Classify this cell by malaria status.
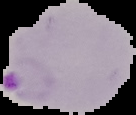

It is parasitized.

Summary:
  - Image type: segmented cell region with the area outside set to black
  - Image size: 136×115 pixels
  - Preparation: thin blood film